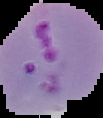
Summary:
  - Preparation: thin blood smear
  - Malaria status: parasitized
  - Image size: 103×118 pixels
  - Image type: segmented cell region with the area outside set to black